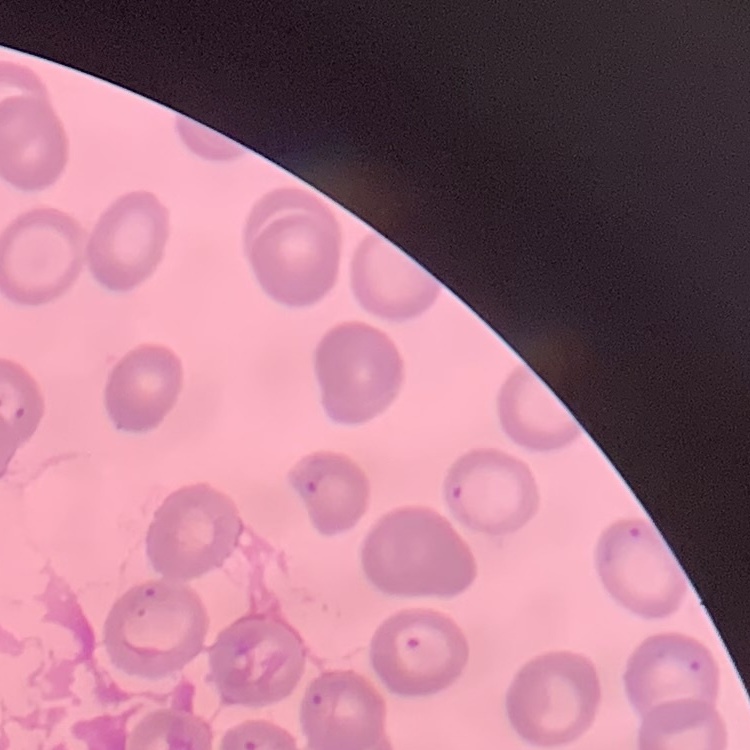
Summary:
  - Red blood cell morphology: no rouleaux formation
  - Image type: square crop of a larger photomicrograph
  - Preparation: thin blood smear
  - Stain: Field's or Giemsa